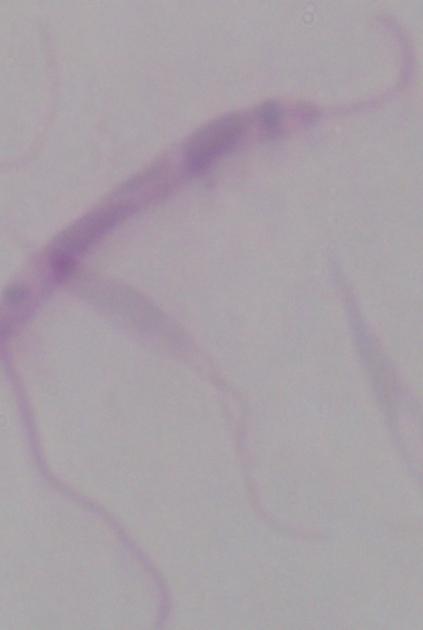

Summary:
  - Identification: Leishmania
  - Modality: photomicrograph
  - Magnification: 1000x